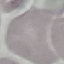

result = negative for malaria parasites
image type = cell patch, automatically extracted from a larger field of view and resized to 64 × 64 pixels
preparation = thin blood smear
capture = smartphone through the microscope eyepiece
stain = Giemsa